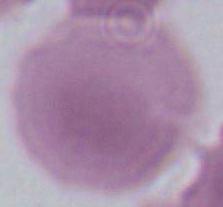

magnification: 1000x
identification: red blood cell
modality: micrograph